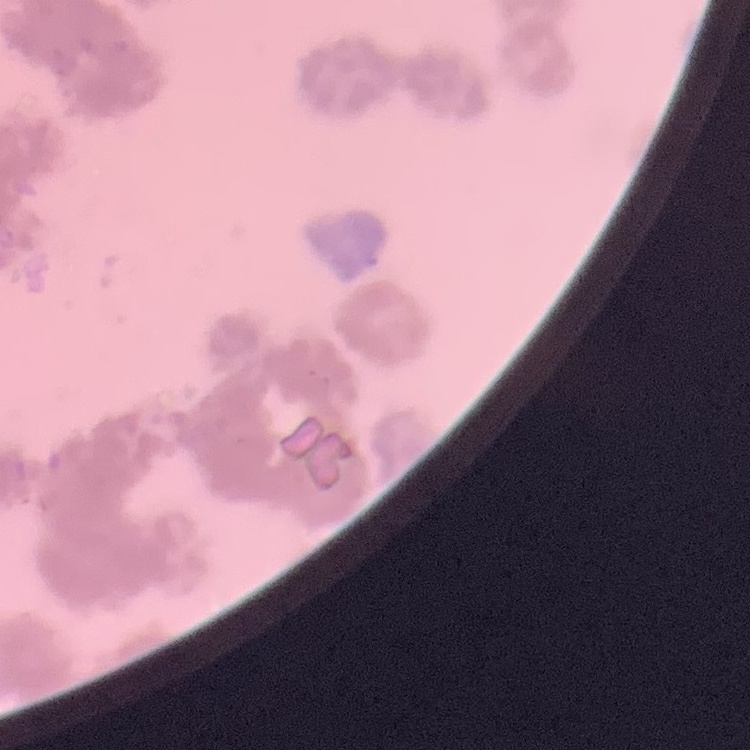 The red blood cells show rouleaux formation. Field's or Giemsa stain. Square crop of a larger photomicrograph. Thin blood film.